Assess this cell for malaria.
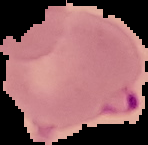

It is parasitized.

image type = cell region segmented out of the field of view; surrounding area masked to black
preparation = thin blood smear
image size = 148×145 pixels